Identify the preparation type.
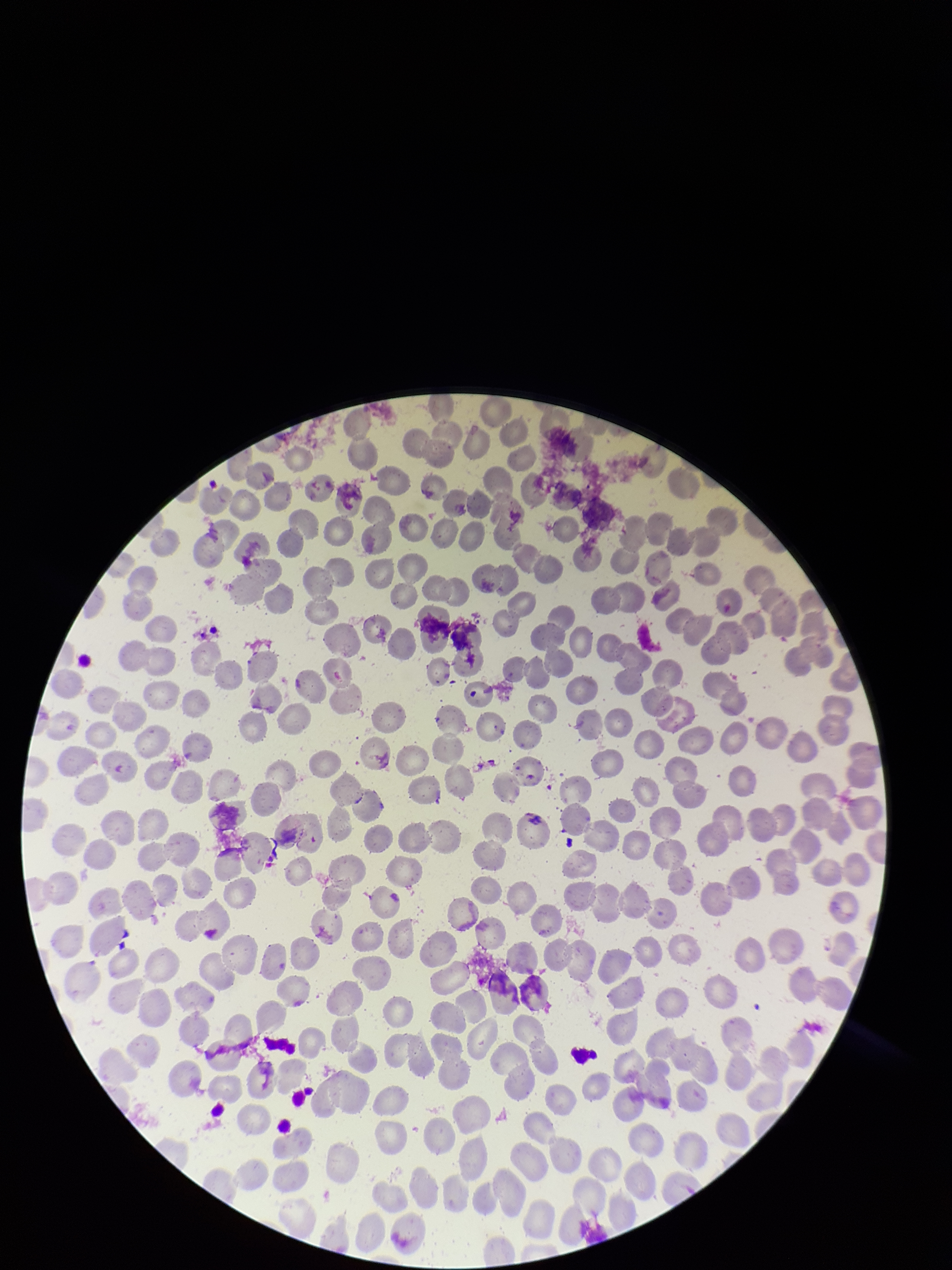

It is a thin blood smear.

{
  "parasitized_red_blood_cells": "none seen",
  "capture": "smartphone photograph through the microscope eyepiece",
  "field_of_view": "one from this slide",
  "image_size": "952×1270 pixels",
  "patient_malaria_status": "negative",
  "red_blood_cell_count": 228,
  "stain": "Giemsa",
  "parasitized_red_blood_cell_count": 0
}